Outline each blood parasite and name the species.
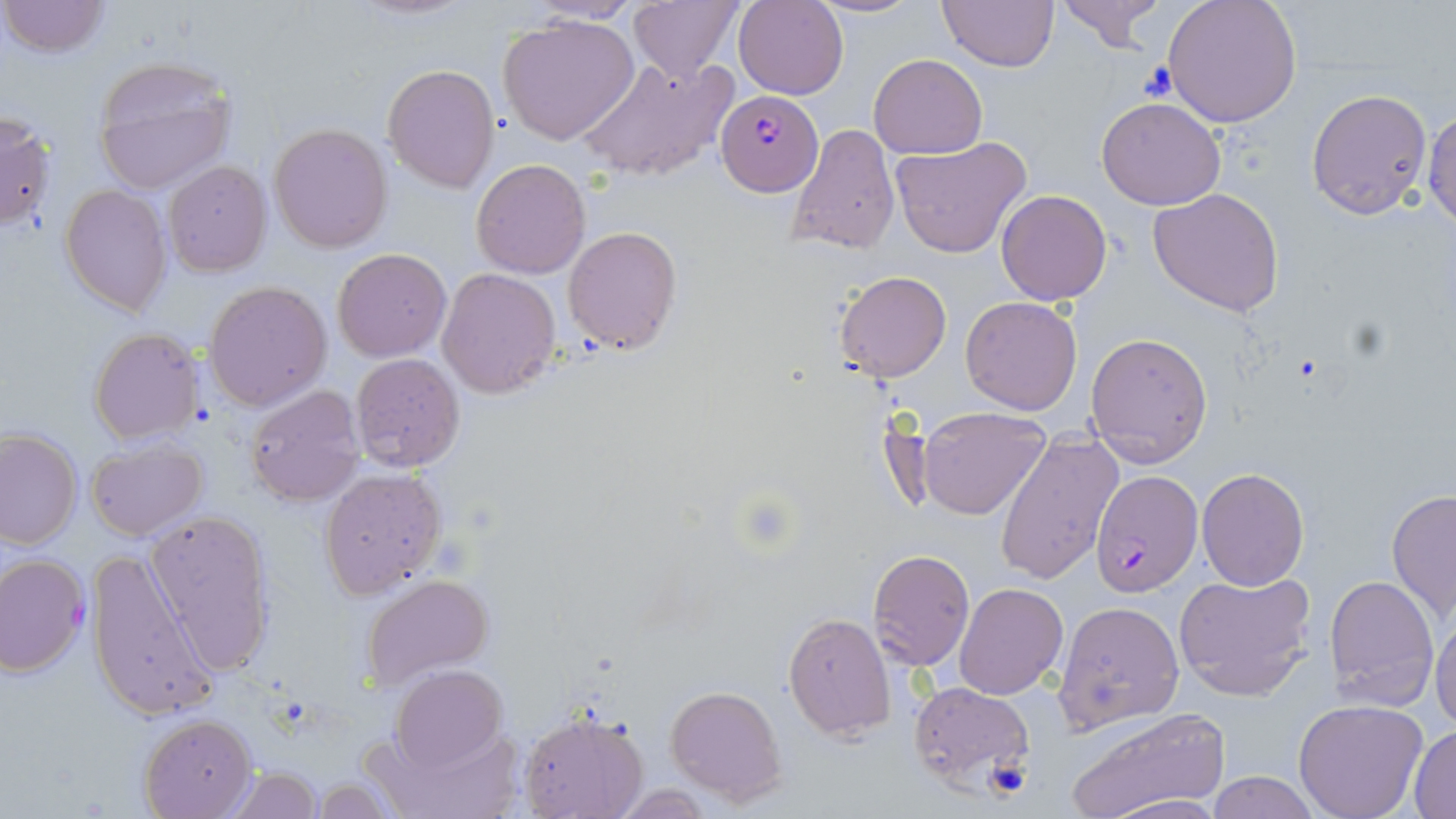
Approximate bounding boxes as [x1, y1, x2, y2] in pixels.
Plasmodium falciparum-infected red blood cells: [716, 91, 822, 197], [1091, 471, 1204, 597].
No Plasmodium ovale, Plasmodium malariae, Plasmodium vivax, Babesia divergens, or Trypanosoma brucei observed.

slide-level diagnosis = Plasmodium falciparum
preparation = thin blood smear
magnification = 1000x
stain = May-Grünwald-Giemsa
field of view = one of a larger specimen
image size = 1456×819 pixels
uninfected red blood cell locations = approximate bounding boxes as [x1, y1, x2, y2] in pixels: [1, 0, 109, 58], [627, 0, 744, 84], [734, 0, 849, 101], [807, 0, 926, 18], [938, 0, 1056, 71], [1054, 0, 1166, 52], [1161, 0, 1303, 128], [496, 13, 640, 146], [869, 53, 988, 158], [577, 55, 739, 184], [91, 56, 237, 196], [384, 63, 499, 192], [1307, 89, 1433, 218], [1096, 96, 1225, 210], [1423, 105, 1456, 229], [0, 111, 57, 234], [270, 123, 393, 252], [787, 124, 900, 256], [888, 136, 1033, 258], [471, 158, 592, 278], [165, 161, 272, 277], [60, 186, 170, 315], [1149, 188, 1284, 317], [996, 189, 1112, 306], [983, 190, 1098, 411], [565, 226, 681, 353], [334, 248, 452, 362], [437, 268, 561, 398], [836, 271, 951, 383], [205, 280, 331, 411], [960, 295, 1082, 415], [89, 327, 204, 444], [1086, 333, 1213, 464], [349, 352, 466, 471], [243, 383, 366, 505], [918, 409, 1050, 521], [0, 428, 81, 550], [996, 436, 1122, 585], [85, 438, 208, 540], [319, 467, 447, 598], [1196, 467, 1309, 590], [1387, 486, 1456, 626], [143, 507, 277, 673], [86, 548, 219, 726], [869, 549, 974, 671], [0, 553, 89, 677], [1174, 569, 1316, 702], [1324, 573, 1440, 711], [361, 574, 493, 689], [954, 582, 1069, 701], [1052, 600, 1186, 734], [1430, 607, 1456, 732], [783, 611, 896, 743], [391, 664, 506, 772], [908, 682, 1036, 793], [666, 684, 787, 807], [1294, 699, 1428, 819], [1063, 706, 1231, 819], [519, 711, 649, 819], [138, 715, 254, 818], [374, 718, 524, 819], [1411, 724, 1456, 818], [223, 765, 322, 819], [1204, 771, 1320, 819], [306, 777, 401, 816], [611, 784, 716, 816], [1094, 792, 1229, 819]
modality = light microscopy
platelet locations = approximate bounding boxes as [x1, y1, x2, y2] in pixels: [1139, 60, 1178, 102], [984, 757, 1033, 800]